Assess this cell for malaria.
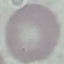
Uninfected.

preparation = thin blood smear
image type = cell patch, automatically extracted from a larger field of view and resized to 64 × 64 pixels
capture = smartphone through the microscope eyepiece
stain = Giemsa